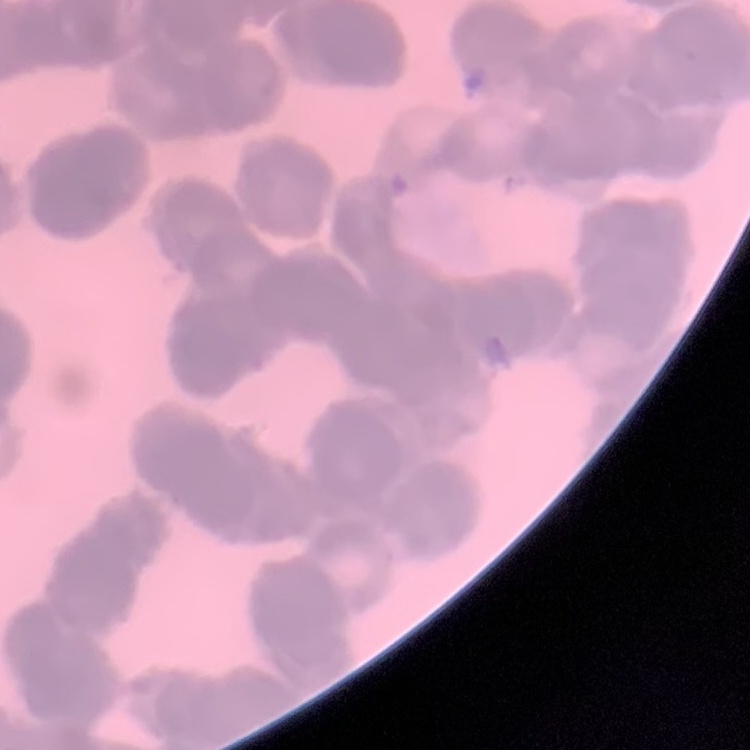

Summary:
  - Erythrocyte morphology: rouleaux formation
  - Stain: Field's or Giemsa
  - Preparation: thin blood smear
  - Image type: square crop of a larger photomicrograph